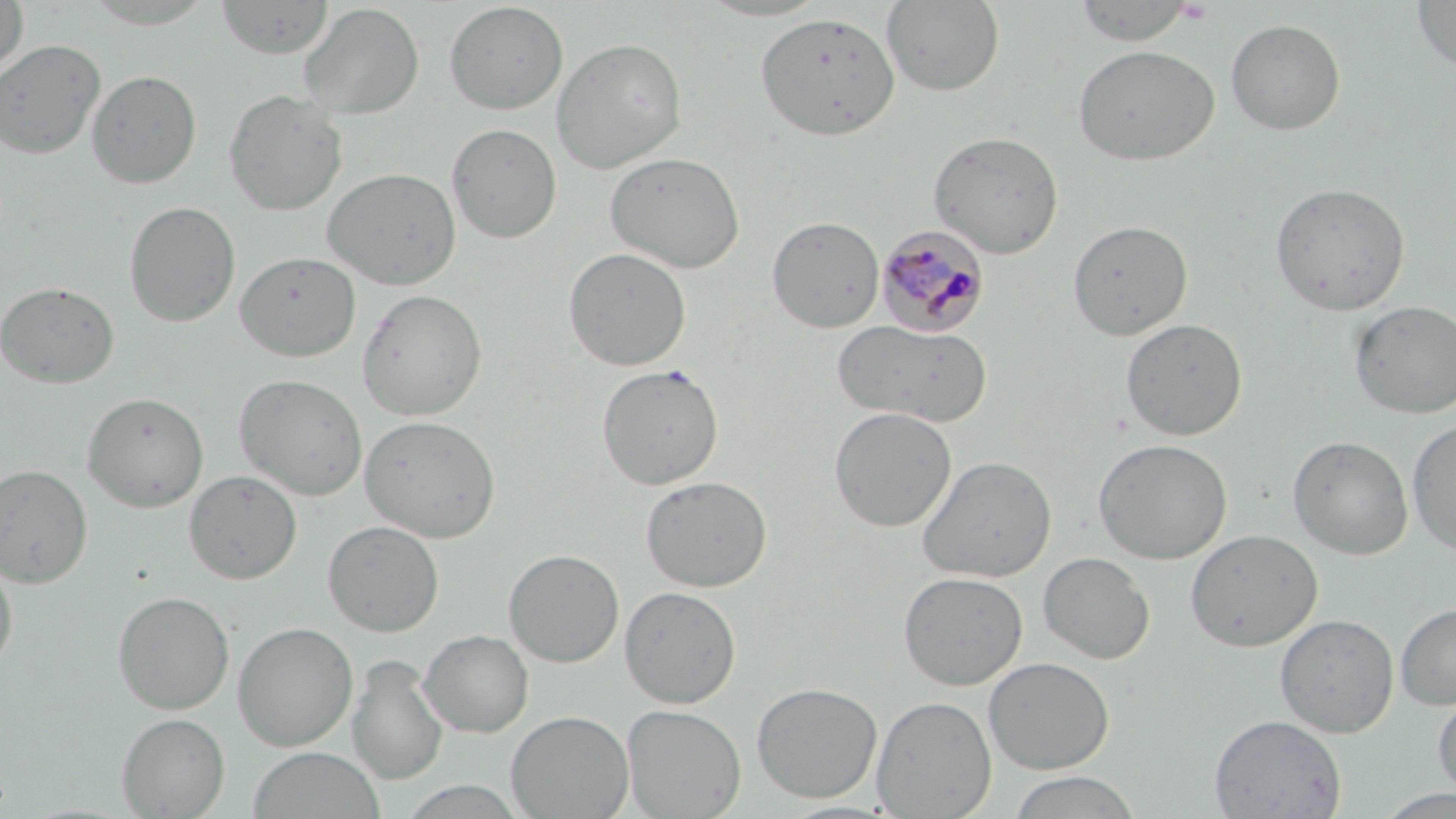

{
  "slide_level_diagnosis": "Plasmodium malariae",
  "platelet_locations": "approximate bounding boxes as (x1,y1)-(x2,y2) corner pairs in pixels: (1175,1)-(1214,24)",
  "stain": "May-Grünwald-Giemsa",
  "preparation": "thin blood smear",
  "image_size": "1456×819 pixels",
  "plasmodium_malariae_infected_red_blood_cell_locations": "approximate bounding boxes as (x1,y1)-(x2,y2) corner pairs in pixels: (875,224)-(989,337)",
  "modality": "light microscopy",
  "uninfected_red_blood_cell_locations": "approximate bounding boxes as (x1,y1)-(x2,y2) corner pairs in pixels: (216,0)-(334,59), (219,0)-(392,88), (695,0)-(836,21), (1410,0)-(1456,73), (0,1)-(29,82), (77,1)-(221,29), (881,1)-(1005,96), (1073,1)-(1196,46), (443,2)-(568,115), (298,3)-(424,119), (754,11)-(900,142), (1226,19)-(1345,136), (550,36)-(688,174), (0,39)-(106,159), (1072,44)-(1220,166), (86,70)-(201,189), (223,88)-(348,217), (447,123)-(562,245), (928,130)-(1064,258), (605,151)-(746,274), (322,167)-(462,290), (1270,182)-(1410,316), (124,201)-(240,328), (767,216)-(885,333), (1067,219)-(1193,341), (563,247)-(691,371), (234,251)-(361,363), (0,280)-(120,389), (357,288)-(487,421), (1349,300)-(1456,420), (1120,318)-(1247,441), (834,319)-(989,427), (596,363)-(725,490), (234,373)-(368,502), (82,391)-(209,512), (828,406)-(957,533), (359,415)-(501,543), (1406,418)-(1456,557), (1288,434)-(1414,560), (1093,439)-(1233,564), (917,455)-(1057,583), (0,464)-(93,588), (184,470)-(302,584), (640,475)-(773,592), (322,520)-(444,637), (1185,529)-(1323,652), (503,549)-(624,668), (1038,552)-(1155,664), (0,553)-(18,676), (897,571)-(1027,690), (619,585)-(741,709), (112,591)-(234,715), (1395,602)-(1456,711), (1274,613)-(1399,738), (232,622)-(358,751), (419,629)-(534,738), (347,653)-(448,787), (983,656)-(1114,775), (750,681)-(882,803), (1432,687)-(1456,801), (871,695)-(996,818), (621,704)-(746,818), (506,710)-(634,818), (116,712)-(230,818), (1209,714)-(1346,818), (248,747)-(385,819), (1006,771)-(1143,818), (396,780)-(528,819), (1374,788)-(1456,818)",
  "magnification": "1000x",
  "field_of_view": "one of a larger specimen"
}